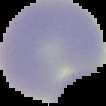 Image is 106×106 pixels. Cell region segmented out of the field of view; the surrounding area is masked to black. From a thin blood film. Malaria status: uninfected.